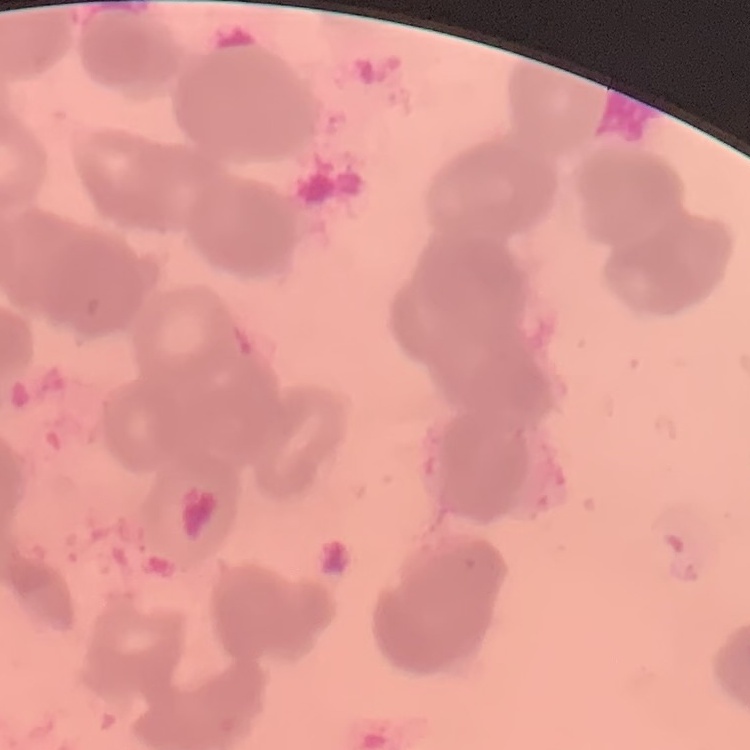

{
  "red_blood_cell_morphology": "rouleaux formation",
  "preparation": "thin blood film",
  "image_type": "square crop of a larger photomicrograph",
  "stain": "Field's or Giemsa"
}